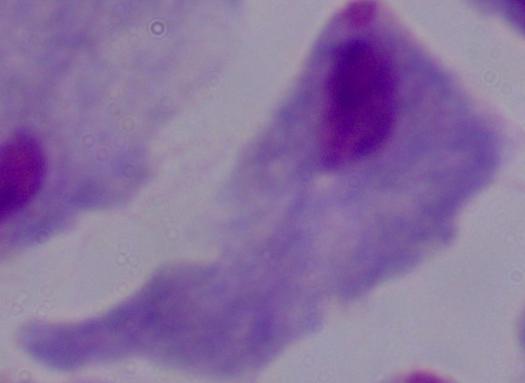

Summary:
  - Modality: photomicrograph
  - Magnification: 1000x
  - Identification: trichomonad